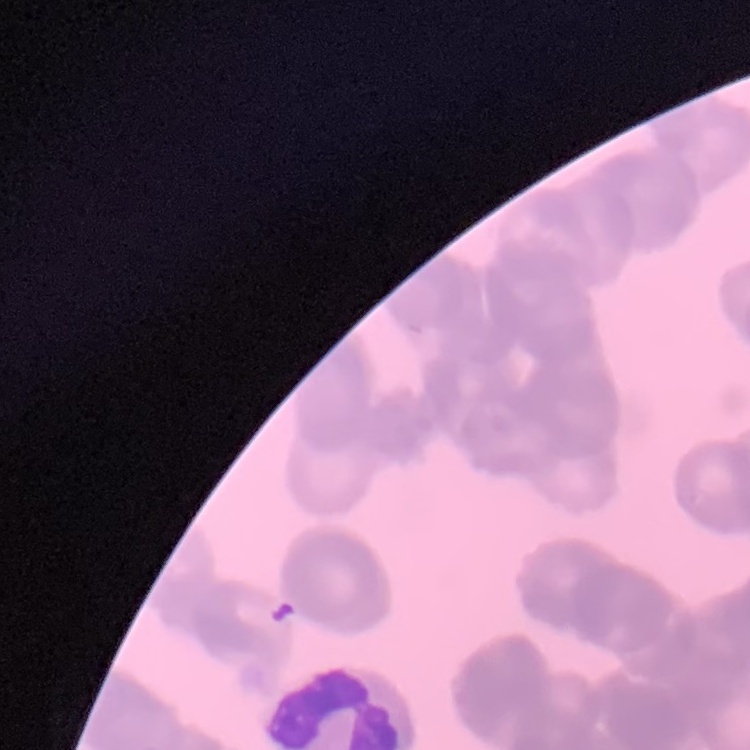

Summary:
  - Erythrocyte morphology: rouleaux formation
  - Stain: Field's or Giemsa
  - Image type: square crop of a larger photomicrograph
  - Preparation: thin peripheral smear